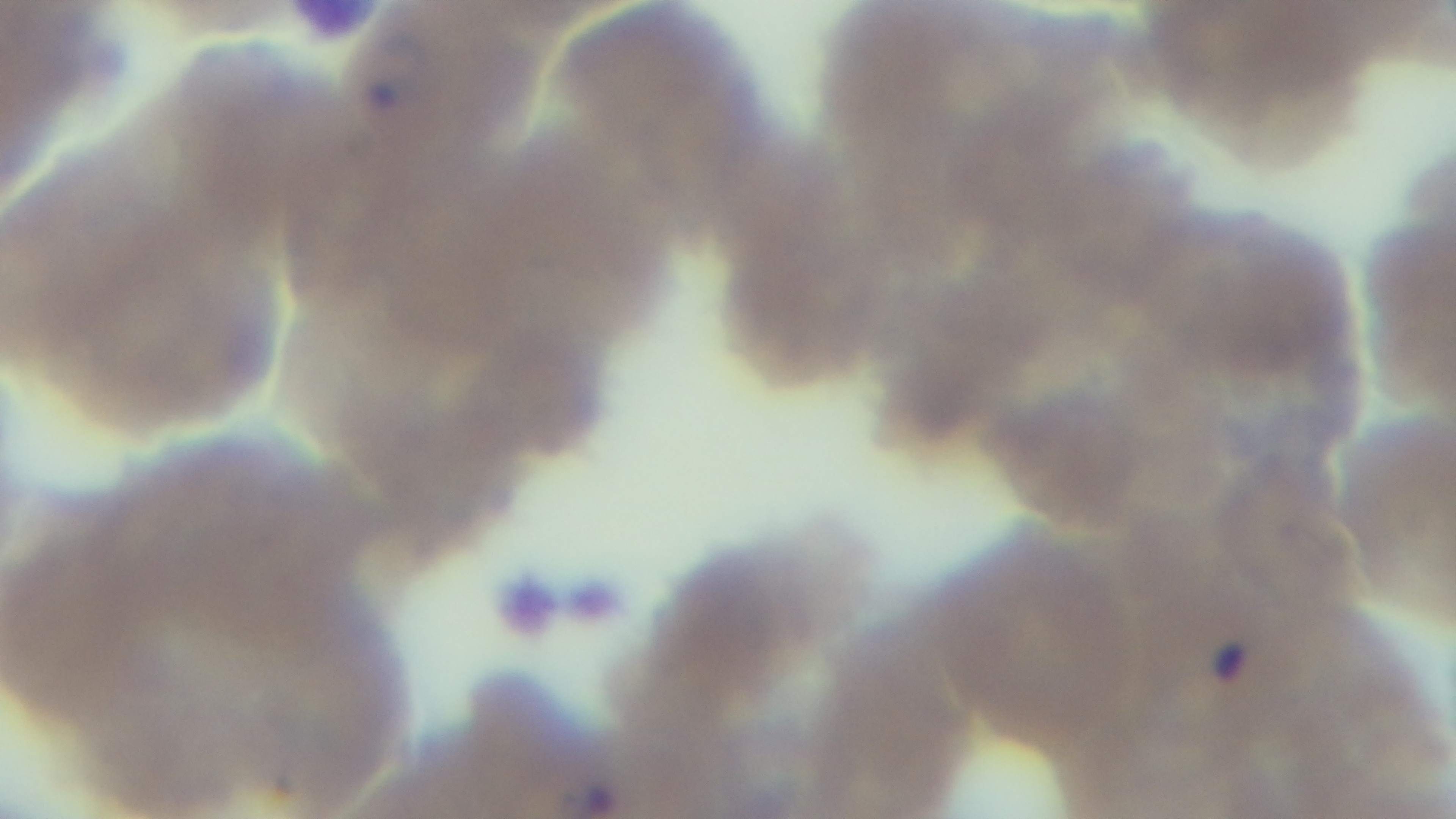

{
  "malaria_status": "infected",
  "objective": "100x oil immersion",
  "preparation": "thin",
  "capture": "mounted 4K digital camera",
  "modality": "light microscopy",
  "stain": "Giemsa",
  "field_of_view": "single"
}